State which parasite is depicted.
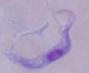

A trypanosome.

modality = photomicrograph
magnification = 1000x